Look for Plasmodium parasites.
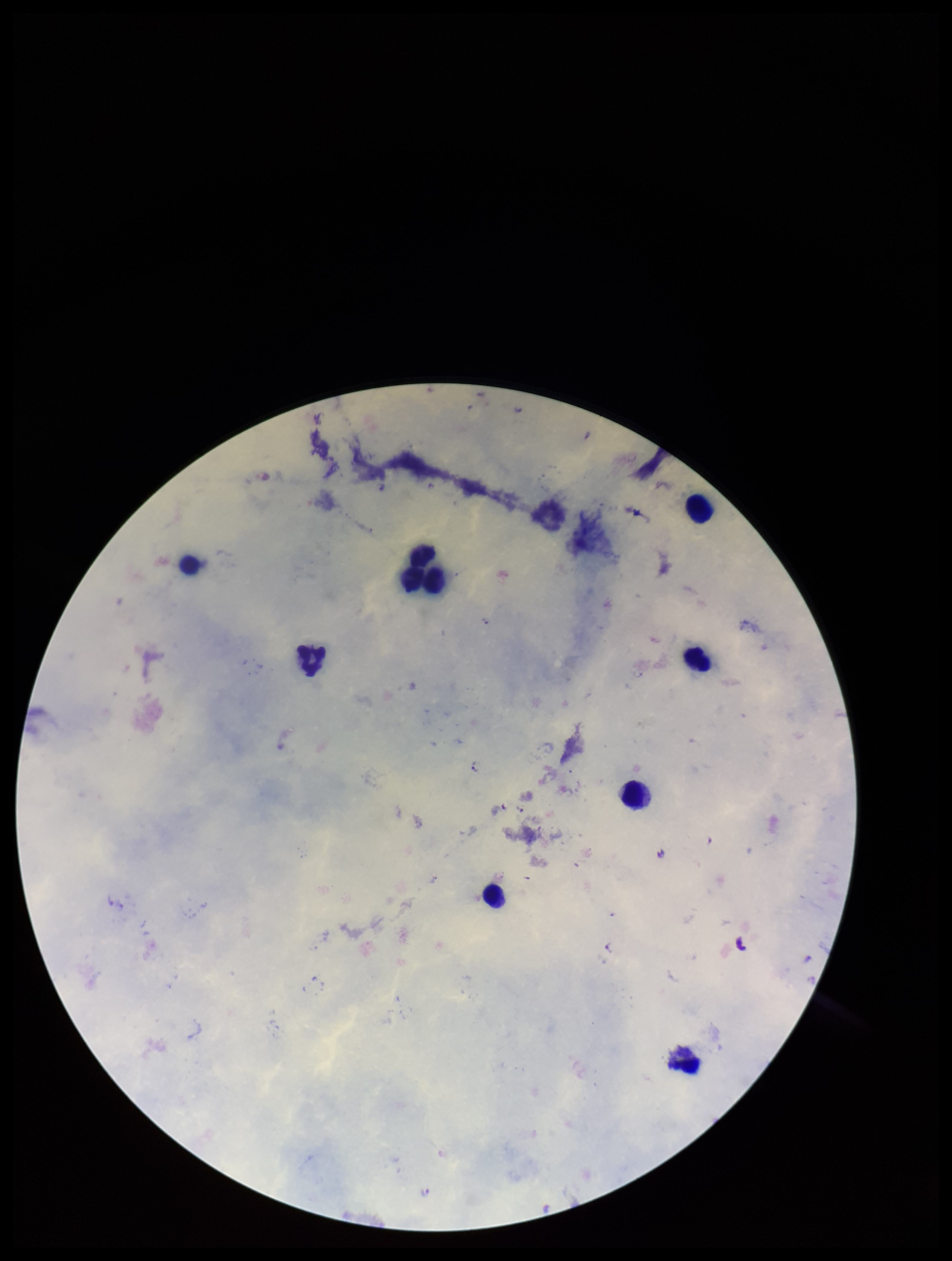
Detected.

Single field of view. Image is 952×1261 pixels. Species reported for this patient: Plasmodium falciparum. Leukocyte count: 8. Patient malaria status: infected. Giemsa stain. Parasite count: 7. Preparation: thick smear. Photographed through the microscope eyepiece with a smartphone camera.